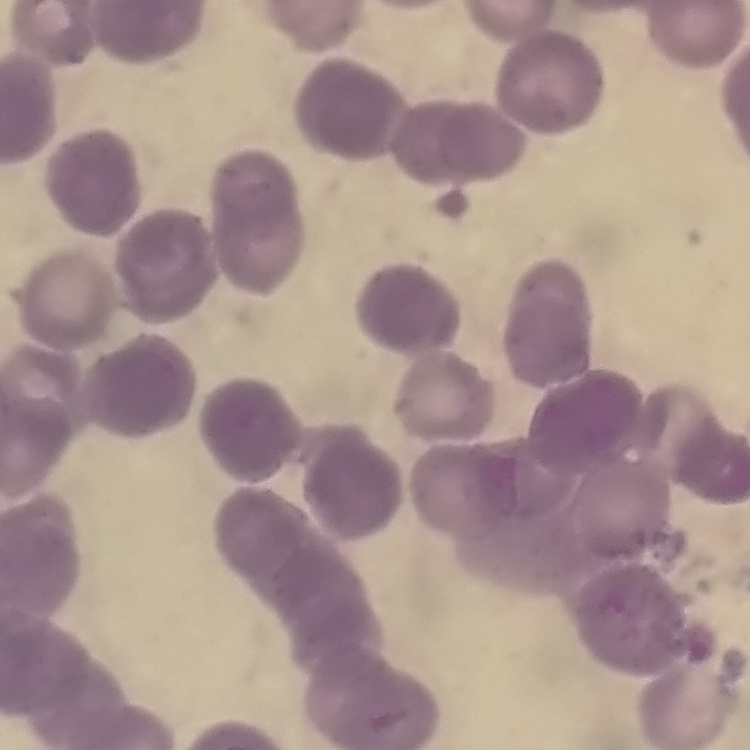

The red blood cells exhibit rouleaux formation. Stained with either Field's or Giemsa. Thin blood smear. One tile cut from a larger photomicrograph.